Identify the parasite.
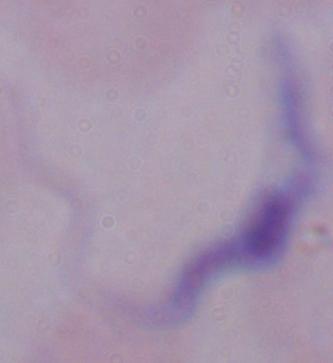

This is a trypanosome.

{
  "modality": "photomicrograph",
  "magnification": "1000x"
}